Report the malaria status of this cell.
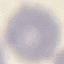

It is uninfected.

Summary:
  - Capture: smartphone through the microscope eyepiece
  - Stain: Giemsa
  - Image type: automatically extracted cell patch, resized to 64 × 64 pixels
  - Preparation: thin smear